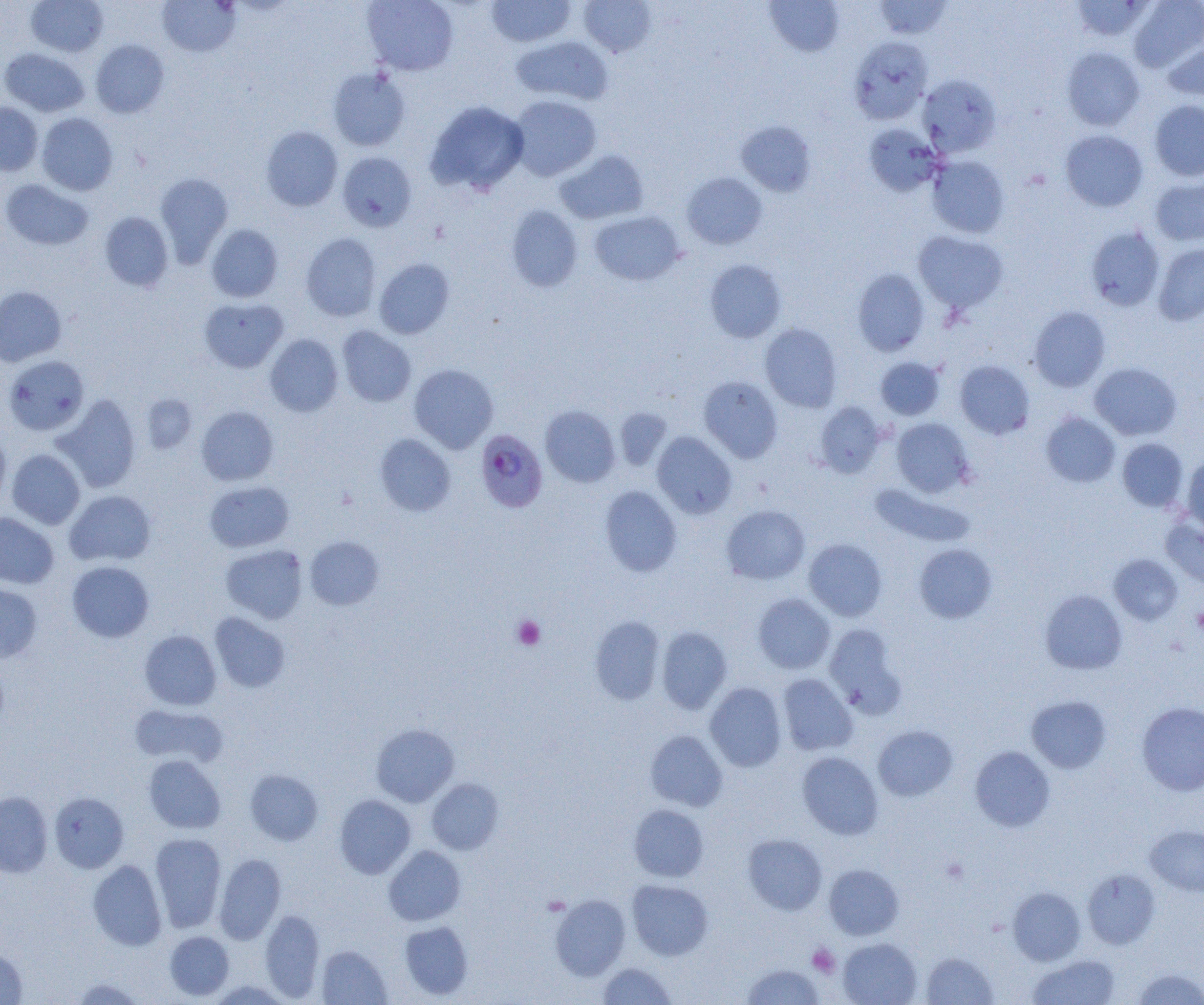
slide-level diagnosis = Plasmodium falciparum
uninfected red blood cell locations = approximate bounding boxes as named x1/y1/x2/y2 corners in pixels: (x1=26, y1=0, x2=108, y2=57), (x1=362, y1=0, x2=459, y2=75), (x1=486, y1=0, x2=575, y2=47), (x1=579, y1=0, x2=657, y2=58), (x1=764, y1=0, x2=845, y2=57), (x1=873, y1=0, x2=952, y2=39), (x1=1070, y1=0, x2=1154, y2=41), (x1=1129, y1=0, x2=1204, y2=72), (x1=157, y1=1, x2=241, y2=57), (x1=1162, y1=35, x2=1204, y2=100), (x1=510, y1=36, x2=613, y2=106), (x1=849, y1=36, x2=932, y2=124), (x1=91, y1=39, x2=169, y2=118), (x1=1062, y1=47, x2=1145, y2=131), (x1=1, y1=48, x2=89, y2=117), (x1=327, y1=66, x2=411, y2=151), (x1=918, y1=74, x2=1001, y2=157), (x1=509, y1=95, x2=601, y2=181), (x1=1149, y1=99, x2=1204, y2=181), (x1=425, y1=101, x2=529, y2=195), (x1=0, y1=102, x2=42, y2=175), (x1=36, y1=113, x2=118, y2=196), (x1=735, y1=121, x2=816, y2=197), (x1=863, y1=124, x2=943, y2=196), (x1=260, y1=126, x2=343, y2=211), (x1=1060, y1=130, x2=1148, y2=212), (x1=554, y1=149, x2=649, y2=224), (x1=337, y1=152, x2=417, y2=232), (x1=927, y1=155, x2=1009, y2=239), (x1=155, y1=172, x2=234, y2=266), (x1=682, y1=172, x2=767, y2=249), (x1=1150, y1=177, x2=1204, y2=246), (x1=1, y1=179, x2=93, y2=251), (x1=506, y1=205, x2=583, y2=292), (x1=589, y1=211, x2=685, y2=286), (x1=99, y1=212, x2=173, y2=292), (x1=206, y1=224, x2=283, y2=302), (x1=1085, y1=225, x2=1164, y2=311), (x1=913, y1=231, x2=1008, y2=313), (x1=300, y1=233, x2=381, y2=321), (x1=1153, y1=243, x2=1204, y2=325), (x1=374, y1=258, x2=455, y2=339), (x1=705, y1=259, x2=786, y2=343), (x1=852, y1=269, x2=929, y2=356), (x1=0, y1=286, x2=66, y2=366), (x1=199, y1=297, x2=288, y2=373), (x1=1029, y1=306, x2=1111, y2=392), (x1=760, y1=324, x2=842, y2=412), (x1=337, y1=326, x2=416, y2=407), (x1=264, y1=334, x2=343, y2=416), (x1=3, y1=355, x2=89, y2=435), (x1=875, y1=357, x2=945, y2=420), (x1=955, y1=360, x2=1035, y2=439), (x1=1089, y1=362, x2=1181, y2=440), (x1=409, y1=364, x2=498, y2=453), (x1=699, y1=376, x2=783, y2=462), (x1=53, y1=394, x2=141, y2=493), (x1=142, y1=394, x2=197, y2=453), (x1=815, y1=402, x2=886, y2=477), (x1=540, y1=405, x2=620, y2=488), (x1=197, y1=406, x2=278, y2=486), (x1=614, y1=408, x2=672, y2=471), (x1=1041, y1=412, x2=1120, y2=488), (x1=891, y1=418, x2=974, y2=497), (x1=0, y1=429, x2=11, y2=512), (x1=652, y1=431, x2=737, y2=519), (x1=374, y1=434, x2=456, y2=516), (x1=1117, y1=438, x2=1188, y2=512), (x1=6, y1=449, x2=85, y2=529), (x1=1182, y1=456, x2=1204, y2=535), (x1=205, y1=481, x2=294, y2=552), (x1=870, y1=483, x2=976, y2=548), (x1=600, y1=486, x2=682, y2=577), (x1=65, y1=490, x2=156, y2=566), (x1=721, y1=505, x2=810, y2=584), (x1=0, y1=512, x2=59, y2=588), (x1=1160, y1=517, x2=1204, y2=591), (x1=304, y1=536, x2=384, y2=610), (x1=803, y1=539, x2=887, y2=621), (x1=221, y1=544, x2=308, y2=624), (x1=914, y1=544, x2=997, y2=623), (x1=1109, y1=554, x2=1183, y2=624), (x1=67, y1=561, x2=154, y2=643), (x1=0, y1=580, x2=42, y2=663), (x1=1040, y1=590, x2=1127, y2=674), (x1=753, y1=593, x2=835, y2=674), (x1=210, y1=612, x2=290, y2=693), (x1=590, y1=616, x2=666, y2=704), (x1=825, y1=624, x2=905, y2=716), (x1=656, y1=627, x2=732, y2=714), (x1=139, y1=630, x2=221, y2=710), (x1=777, y1=674, x2=857, y2=755), (x1=705, y1=682, x2=786, y2=771), (x1=1026, y1=695, x2=1111, y2=774), (x1=1137, y1=702, x2=1204, y2=795), (x1=130, y1=703, x2=229, y2=769), (x1=371, y1=723, x2=459, y2=806), (x1=873, y1=725, x2=957, y2=801), (x1=645, y1=730, x2=727, y2=812), (x1=970, y1=746, x2=1055, y2=832), (x1=797, y1=752, x2=883, y2=839), (x1=143, y1=755, x2=225, y2=833), (x1=245, y1=769, x2=323, y2=846), (x1=426, y1=778, x2=503, y2=855), (x1=0, y1=791, x2=52, y2=877), (x1=49, y1=792, x2=129, y2=873), (x1=334, y1=795, x2=416, y2=879), (x1=628, y1=804, x2=708, y2=882), (x1=1145, y1=825, x2=1204, y2=896), (x1=150, y1=833, x2=227, y2=933), (x1=743, y1=833, x2=827, y2=915), (x1=383, y1=845, x2=466, y2=925), (x1=214, y1=854, x2=286, y2=944), (x1=88, y1=860, x2=167, y2=950), (x1=824, y1=864, x2=903, y2=940), (x1=1083, y1=869, x2=1160, y2=949), (x1=627, y1=880, x2=713, y2=960), (x1=1008, y1=887, x2=1085, y2=965), (x1=550, y1=894, x2=631, y2=980), (x1=259, y1=908, x2=325, y2=1001), (x1=399, y1=920, x2=473, y2=1000), (x1=165, y1=931, x2=234, y2=1000), (x1=838, y1=938, x2=922, y2=1005), (x1=317, y1=945, x2=392, y2=1004), (x1=0, y1=948, x2=28, y2=1004), (x1=921, y1=952, x2=998, y2=1004), (x1=1027, y1=954, x2=1120, y2=1004), (x1=598, y1=962, x2=676, y2=1005), (x1=742, y1=964, x2=824, y2=1004), (x1=1132, y1=968, x2=1204, y2=1005), (x1=69, y1=977, x2=146, y2=1005), (x1=208, y1=980, x2=291, y2=1005)
Plasmodium falciparum-infected red blood cell locations = approximate bounding boxes as named x1/y1/x2/y2 corners in pixels: (x1=475, y1=429, x2=548, y2=512)
field of view = one of a larger specimen
magnification = 1000x
platelet locations = approximate bounding boxes as named x1/y1/x2/y2 corners in pixels: (x1=1192, y1=606, x2=1204, y2=636), (x1=513, y1=616, x2=545, y2=649), (x1=941, y1=857, x2=969, y2=884), (x1=807, y1=944, x2=841, y2=978)
image size = 1204×1005 pixels
preparation = thin blood smear
modality = optical microscopy